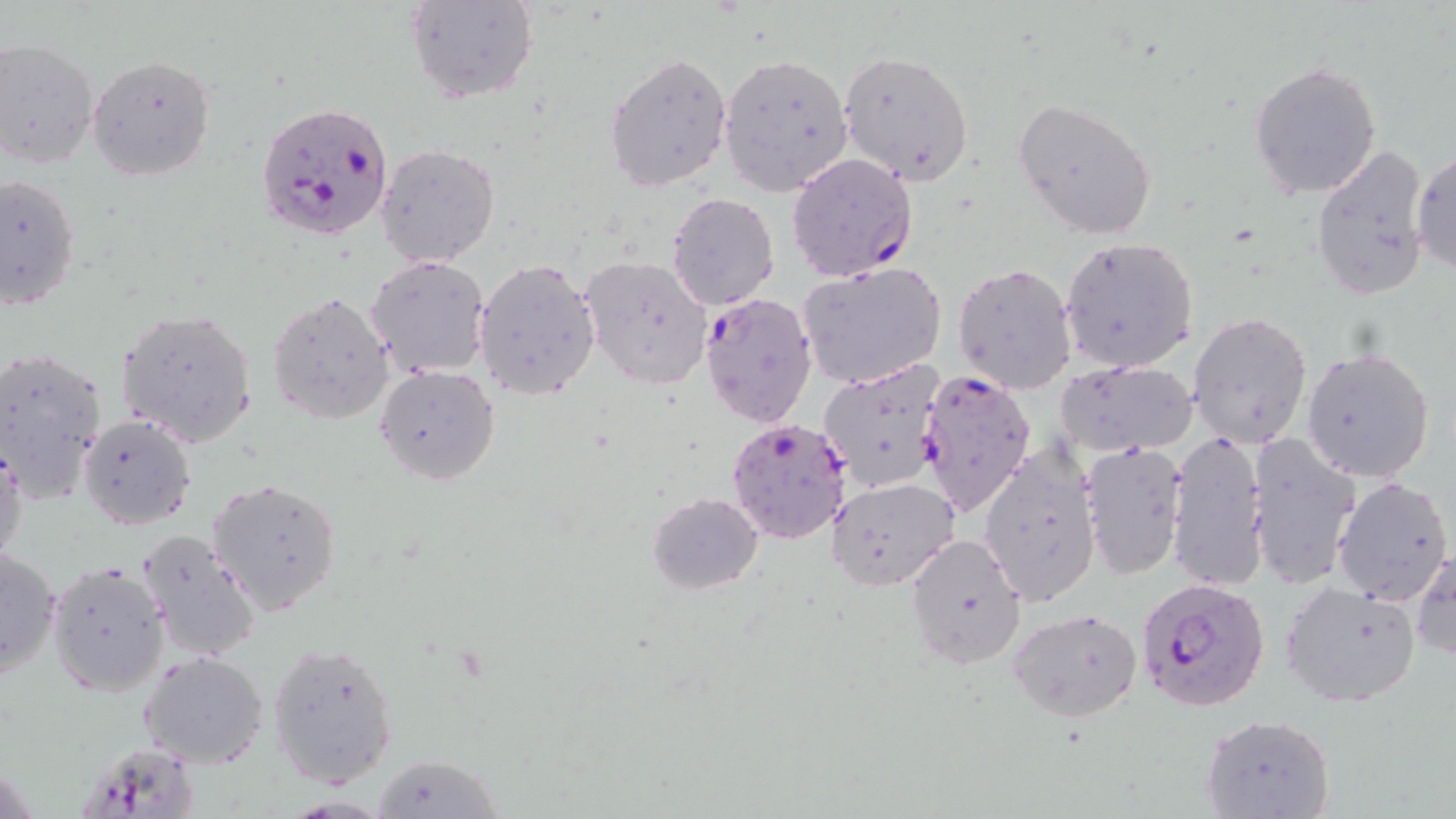
slide-level diagnosis = Plasmodium falciparum
modality = light microscopy
uninfected red blood cell locations = approximate bounding boxes as named x1/y1/x2/y2 corners in pixels: (x1=405, y1=0, x2=540, y2=106), (x1=0, y1=38, x2=100, y2=168), (x1=838, y1=51, x2=974, y2=184), (x1=605, y1=52, x2=733, y2=190), (x1=718, y1=52, x2=854, y2=195), (x1=86, y1=55, x2=217, y2=181), (x1=1249, y1=60, x2=1381, y2=198), (x1=1012, y1=97, x2=1158, y2=240), (x1=376, y1=142, x2=501, y2=268), (x1=1310, y1=143, x2=1432, y2=299), (x1=1410, y1=149, x2=1455, y2=276), (x1=0, y1=172, x2=81, y2=310), (x1=667, y1=192, x2=779, y2=310), (x1=1059, y1=237, x2=1199, y2=373), (x1=365, y1=254, x2=492, y2=378), (x1=579, y1=255, x2=711, y2=390), (x1=473, y1=258, x2=601, y2=400), (x1=798, y1=261, x2=947, y2=391), (x1=953, y1=262, x2=1077, y2=395), (x1=268, y1=292, x2=395, y2=425), (x1=116, y1=309, x2=258, y2=448), (x1=1187, y1=311, x2=1313, y2=448), (x1=1301, y1=346, x2=1436, y2=482), (x1=0, y1=347, x2=108, y2=502), (x1=1055, y1=359, x2=1198, y2=457), (x1=375, y1=363, x2=501, y2=486), (x1=818, y1=364, x2=948, y2=496), (x1=77, y1=412, x2=196, y2=530), (x1=1166, y1=428, x2=1266, y2=594), (x1=1247, y1=433, x2=1362, y2=590), (x1=0, y1=437, x2=26, y2=567), (x1=1082, y1=441, x2=1187, y2=580), (x1=980, y1=443, x2=1101, y2=605), (x1=828, y1=476, x2=960, y2=591), (x1=1332, y1=476, x2=1453, y2=607), (x1=208, y1=478, x2=345, y2=615), (x1=646, y1=491, x2=763, y2=594), (x1=136, y1=530, x2=263, y2=661), (x1=905, y1=531, x2=1029, y2=671), (x1=1, y1=544, x2=61, y2=681), (x1=1411, y1=548, x2=1455, y2=660), (x1=47, y1=560, x2=170, y2=696), (x1=1280, y1=580, x2=1422, y2=709), (x1=1009, y1=607, x2=1144, y2=721), (x1=268, y1=639, x2=400, y2=787), (x1=138, y1=650, x2=269, y2=769), (x1=1199, y1=713, x2=1335, y2=819), (x1=371, y1=754, x2=505, y2=818)
image size = 1456×819 pixels
preparation = thin blood film
magnification = 1000x
Plasmodium falciparum-infected red blood cell locations = approximate bounding boxes as named x1/y1/x2/y2 corners in pixels: (x1=255, y1=99, x2=396, y2=242), (x1=786, y1=152, x2=916, y2=283), (x1=699, y1=292, x2=817, y2=428), (x1=914, y1=368, x2=1036, y2=517), (x1=727, y1=418, x2=854, y2=549), (x1=1136, y1=573, x2=1268, y2=711), (x1=76, y1=747, x2=198, y2=819)
field of view = one of a larger specimen
stain = May-Grünwald-Giemsa